Report the malaria status of this cell.
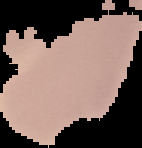
It is uninfected.

Image is 142×148 pixels. From a thin blood smear. Cell region segmented out of the field of view; the surrounding area is masked to black.